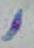
Toxoplasma gondii is shown. Captured at 1000x magnification. Micrograph.